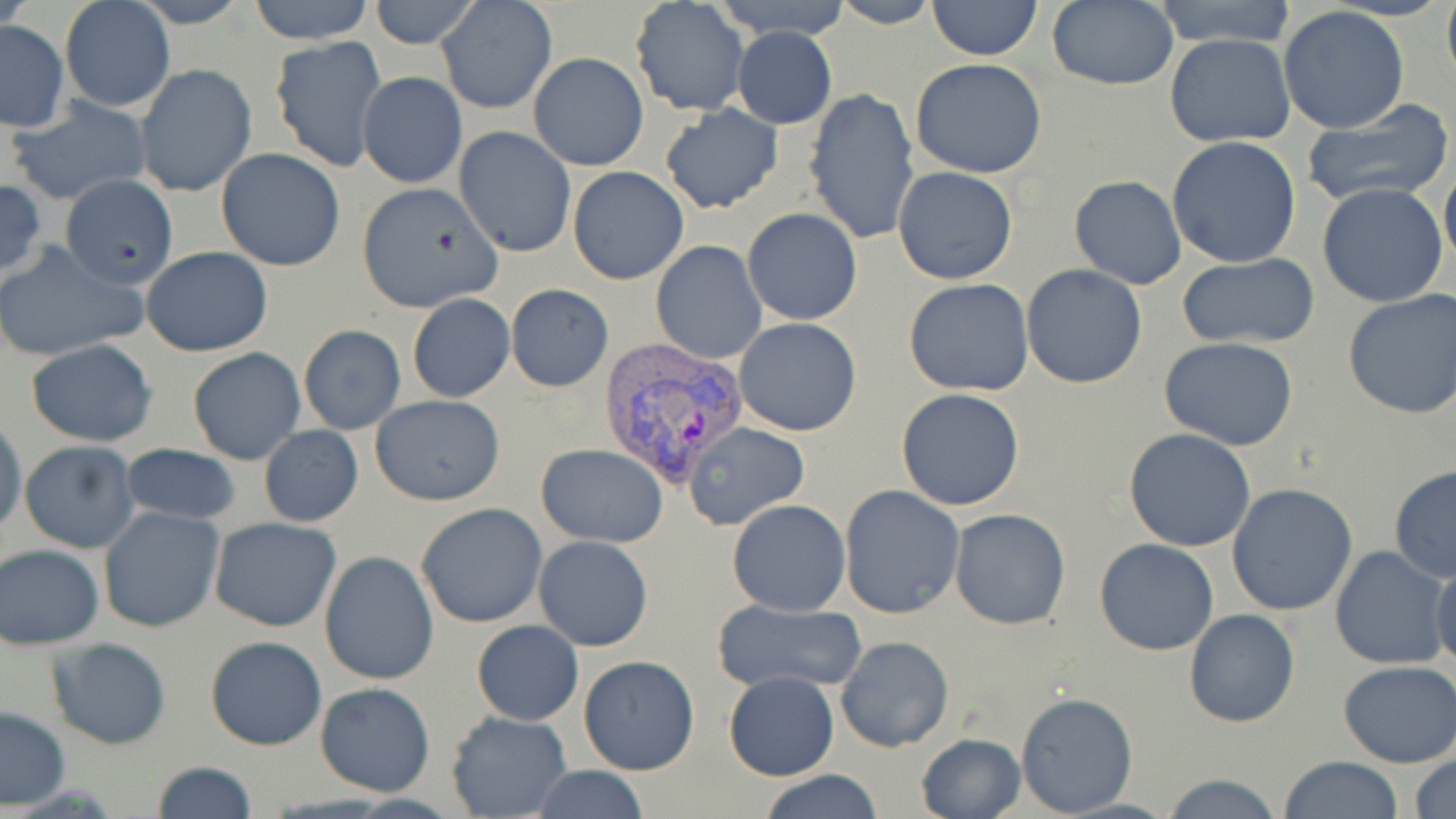

Approximate bounding boxes as (x1, y1, x2, y2) in pixels. Plasmodium vivax-infected red blood cell locations: (595, 335, 751, 489). Uninfected red blood cell locations: (59, 0, 175, 114), (127, 0, 252, 28), (247, 0, 376, 45), (367, 0, 479, 49), (436, 0, 558, 116), (630, 0, 749, 117), (829, 0, 939, 29), (1150, 0, 1301, 50), (1441, 0, 1456, 94), (928, 1, 1042, 60), (1045, 1, 1178, 90), (1278, 5, 1409, 134), (0, 20, 68, 131), (731, 27, 837, 129), (1165, 33, 1295, 147), (268, 35, 387, 173), (529, 51, 649, 170), (909, 57, 1047, 178), (134, 64, 258, 197), (357, 71, 467, 190), (804, 87, 920, 245), (6, 96, 152, 207), (659, 104, 783, 213), (1301, 106, 1454, 208), (453, 126, 576, 257), (1166, 137, 1301, 268), (215, 149, 347, 270), (1441, 162, 1456, 269), (567, 165, 690, 284), (892, 165, 1019, 284), (62, 173, 178, 287), (1068, 175, 1187, 289), (356, 182, 503, 313), (1318, 184, 1447, 308), (742, 207, 862, 325), (0, 239, 147, 361), (651, 240, 766, 365), (140, 246, 273, 356), (1173, 254, 1322, 350), (1021, 264, 1148, 389), (904, 278, 1035, 395), (505, 284, 613, 392), (1342, 289, 1456, 419), (407, 294, 515, 402), (734, 317, 863, 437), (298, 325, 405, 435), (1158, 337, 1300, 453), (26, 340, 158, 448), (188, 347, 306, 465), (896, 387, 1025, 511), (370, 394, 507, 506), (0, 413, 26, 540), (682, 420, 810, 532), (703, 422, 830, 611), (259, 424, 363, 527), (1123, 429, 1258, 551), (18, 440, 142, 552), (118, 444, 239, 526), (535, 444, 668, 547), (1388, 466, 1456, 582), (1227, 483, 1359, 616), (839, 484, 965, 618), (727, 499, 851, 615), (416, 503, 548, 629), (98, 505, 225, 634), (950, 509, 1071, 629), (209, 517, 341, 633), (534, 535, 653, 650), (1095, 539, 1220, 655), (1, 544, 105, 649), (1330, 545, 1451, 668), (321, 551, 439, 686), (1430, 556, 1456, 674), (712, 599, 865, 693), (1185, 609, 1300, 728), (471, 620, 583, 725), (205, 635, 325, 750), (835, 636, 954, 753), (47, 638, 172, 750), (579, 655, 698, 776), (1338, 661, 1456, 767), (723, 671, 839, 781), (314, 682, 436, 797), (1016, 691, 1136, 817), (0, 706, 70, 808), (445, 710, 571, 819), (916, 733, 1026, 818), (1410, 753, 1456, 819), (1277, 756, 1405, 818), (148, 760, 255, 819), (529, 765, 651, 819), (757, 770, 884, 819), (1158, 773, 1286, 818). Slide-level diagnosis: Plasmodium vivax. Single field of view. Light microscopy. Thin blood smear. Image is 1456×819 pixels. May-Grünwald-Giemsa-stained preparation. Captured at 1000x magnification.